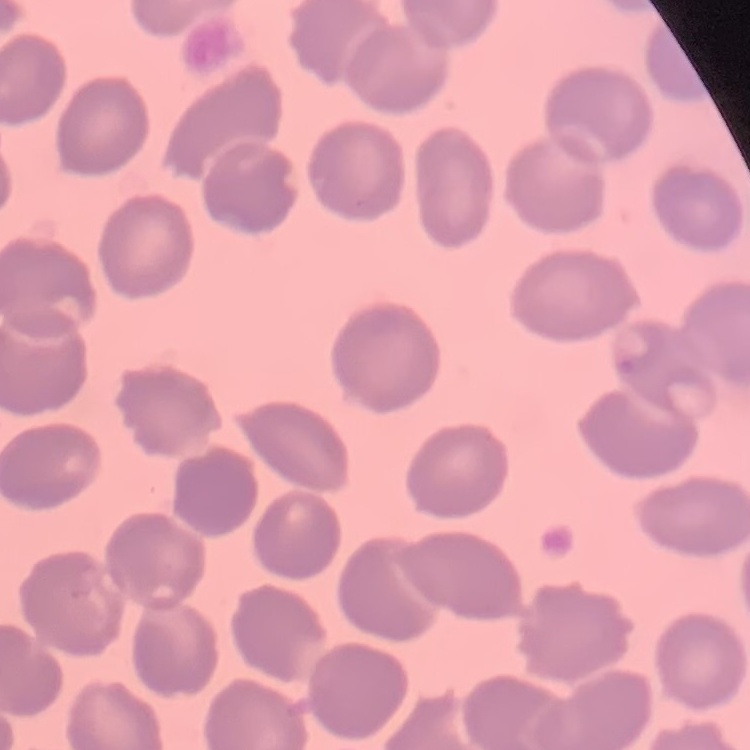
red blood cell morphology = no rouleaux formation
stain = Field's or Giemsa
image type = one tile cut from a larger photomicrograph
preparation = thin blood smear